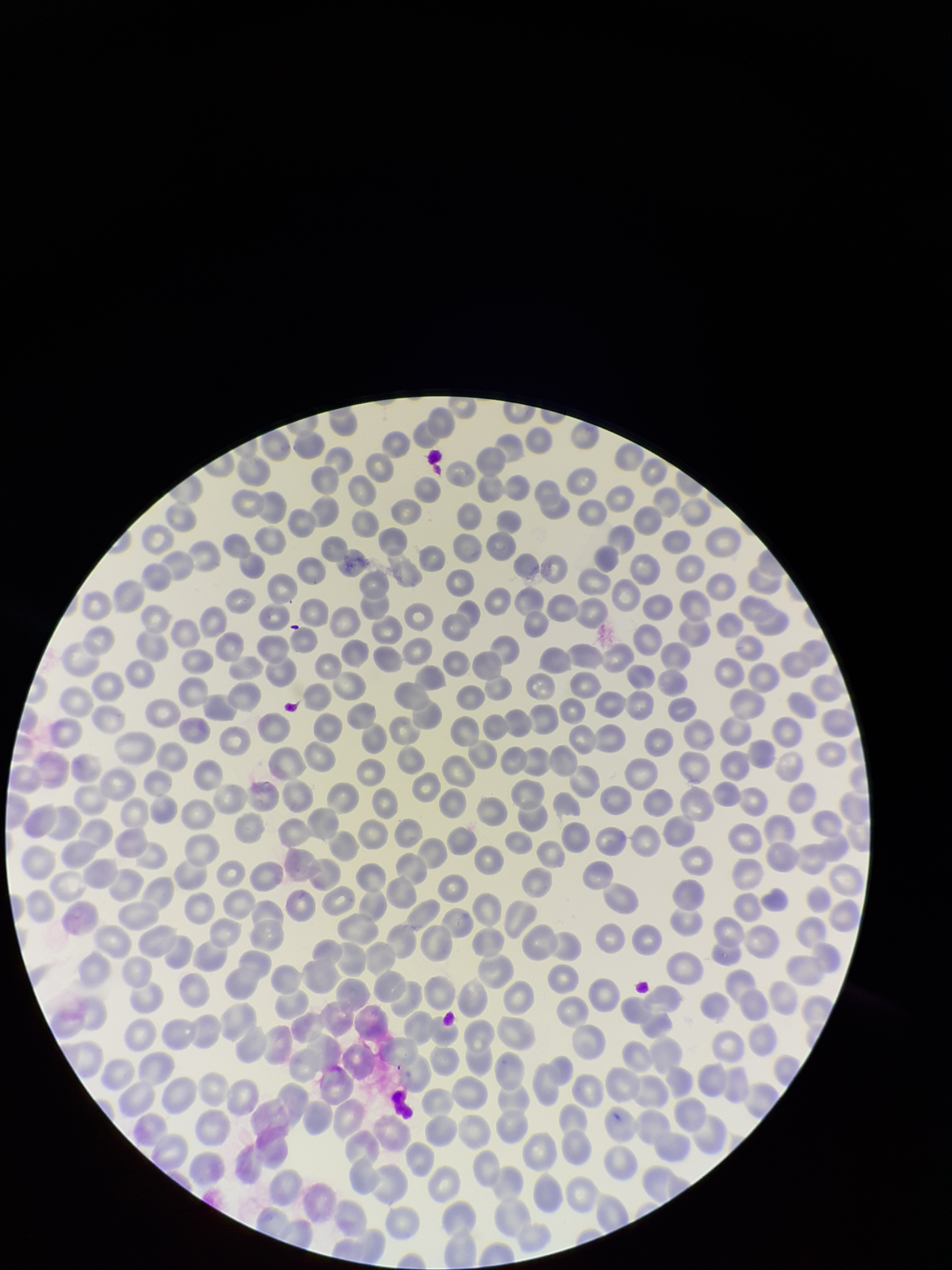
{
  "parasitized_red_blood_cell_count": 0,
  "preparation": "thin",
  "red_blood_cell_count": 350,
  "stain": "Giemsa",
  "parasitized_red_blood_cells": "none detected",
  "species_reported_for_this_patient": "Plasmodium falciparum",
  "image_size": "952×1270 pixels",
  "capture": "smartphone photograph through the microscope eyepiece",
  "field_of_view": "single",
  "patient_malaria_status": "positive"
}